Assess the morphology of the erythrocytes.
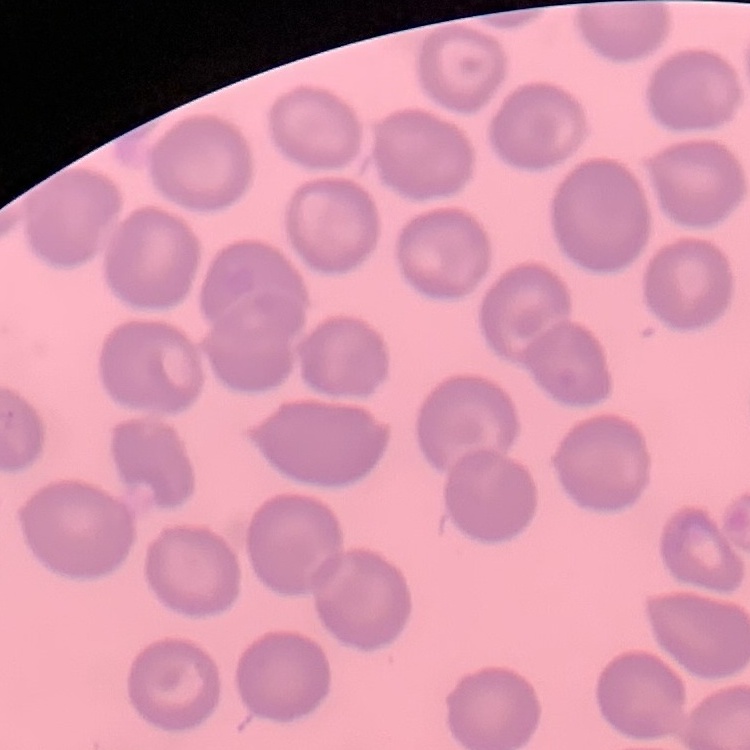
No rouleaux formation.

Summary:
  - Preparation: thin blood smear
  - Stain: Field's or Giemsa
  - Image type: one tile cut from a larger photomicrograph